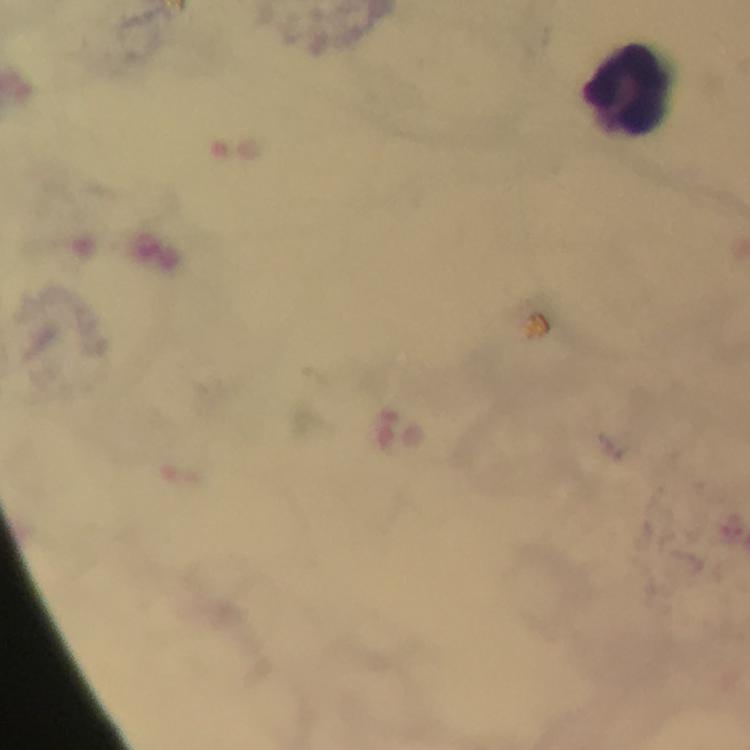
leukocyte_locations: 'approximate centers as (x, y) in pixels: (625, 91)'
capture: smartphone mounted on the microscope
malaria_parasites: none detected
context: from a diagnostic examination for malaria
preparation: thick smear
cropped_from: one field of view
image_size: 750×750 pixels
stain: Giemsa
immersion_oil: used
magnification: 100x